State which parasite is depicted.
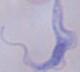
This is a trypanosome.

Photomicrograph. 1000x magnification.